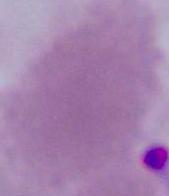

Micrograph. 1000x magnification. An erythrocyte is seen.